State which cell type is depicted.
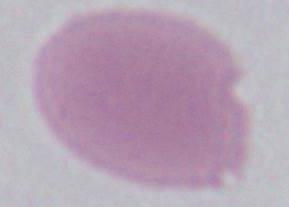
An erythrocyte.

Summary:
  - Magnification: 1000x
  - Modality: micrograph